State which cell type is depicted.
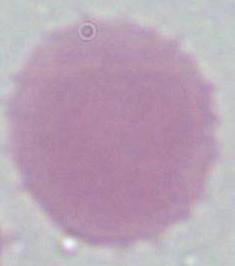
This is an erythrocyte.

Micrograph. 1000x magnification.